Assess the morphology of the erythrocytes.
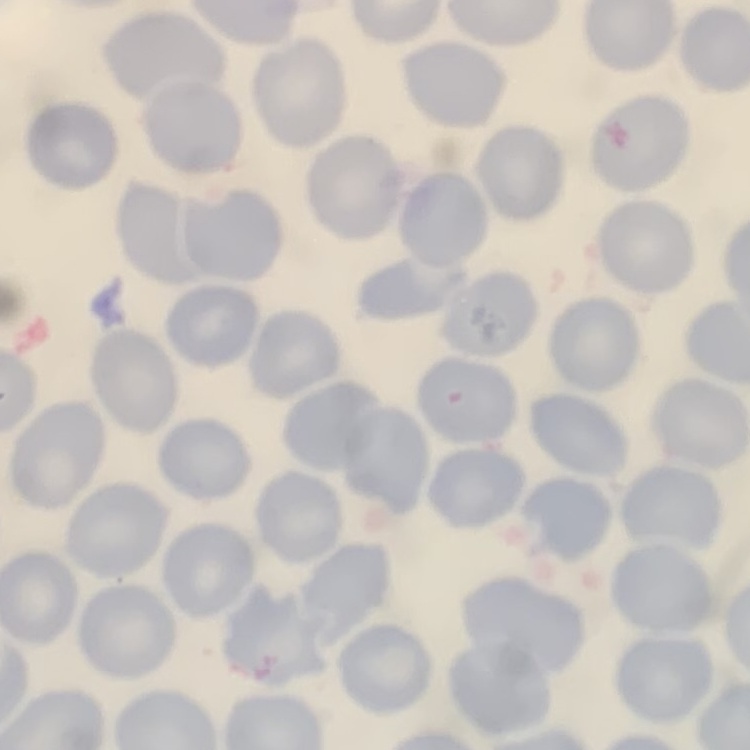

No rouleaux formation.

One tile cut from a larger photomicrograph. Thin blood smear. Field's or Giemsa stain.